Locate every Plasmodium parasite.
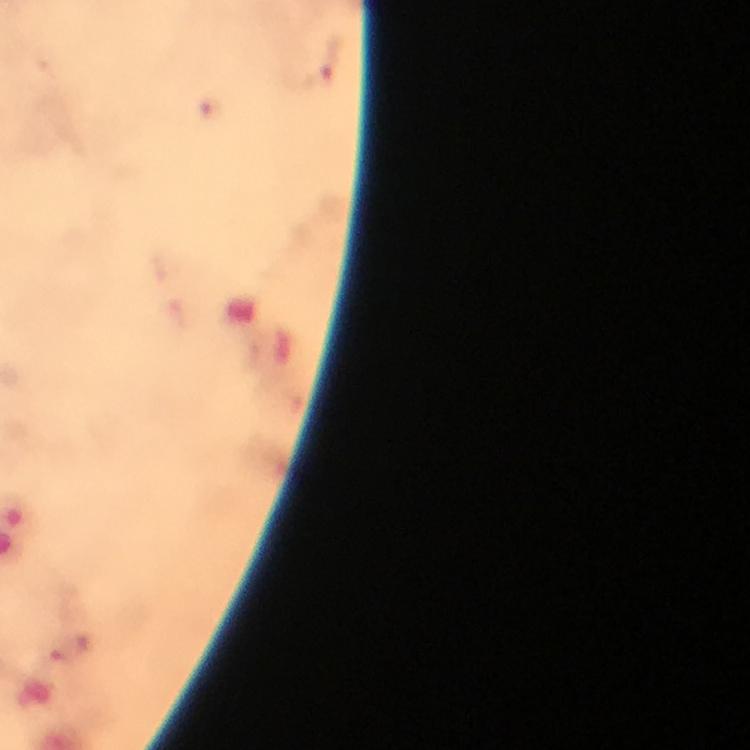

Approximate centers as [x, y] in pixels.
Plasmodium parasites: [331, 58], [212, 108].

Summary:
  - Magnification: 100x
  - Stain: Giemsa
  - Immersion oil: applied
  - Cropped from: a single field of view
  - Preparation: thick blood film
  - Image size: 750×750 pixels
  - Context: from a malaria diagnostic workup
  - Capture: smartphone photograph through a microscope